Describe the morphology of the red blood cells.
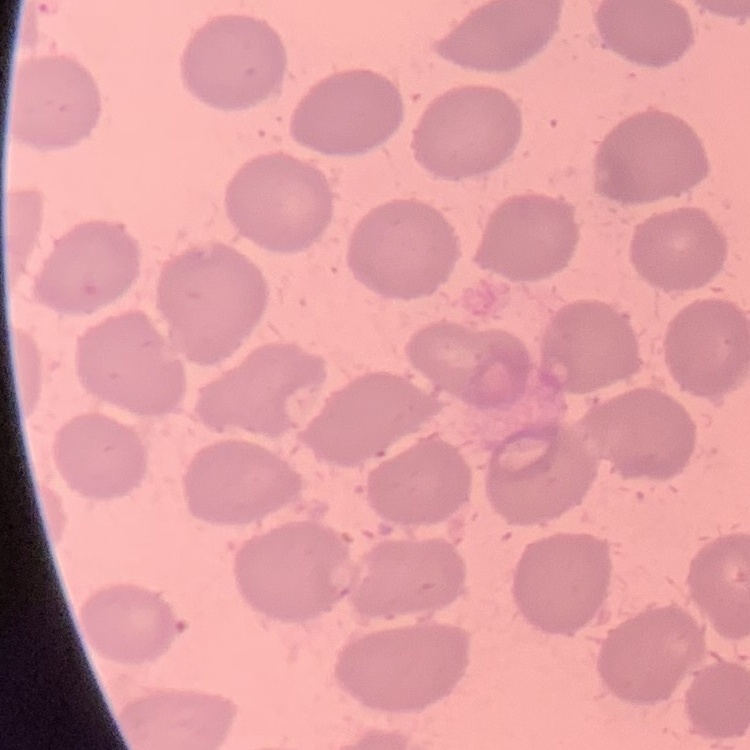
They show no rouleaux formation.

image_type: square crop of a larger photomicrograph
preparation: thin blood film
stain: Field's or Giemsa